Classify this cell by malaria status.
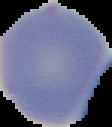

Uninfected.

From a thin blood film. Image is 112×127 pixels. The area outside the segmented cell region is set to black.